Report the malaria status of this cell.
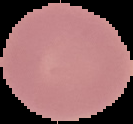
It is uninfected.

Summary:
  - Preparation: thin blood film
  - Image size: 133×124 pixels
  - Image type: cell region segmented out of the field of view; surrounding area masked to black